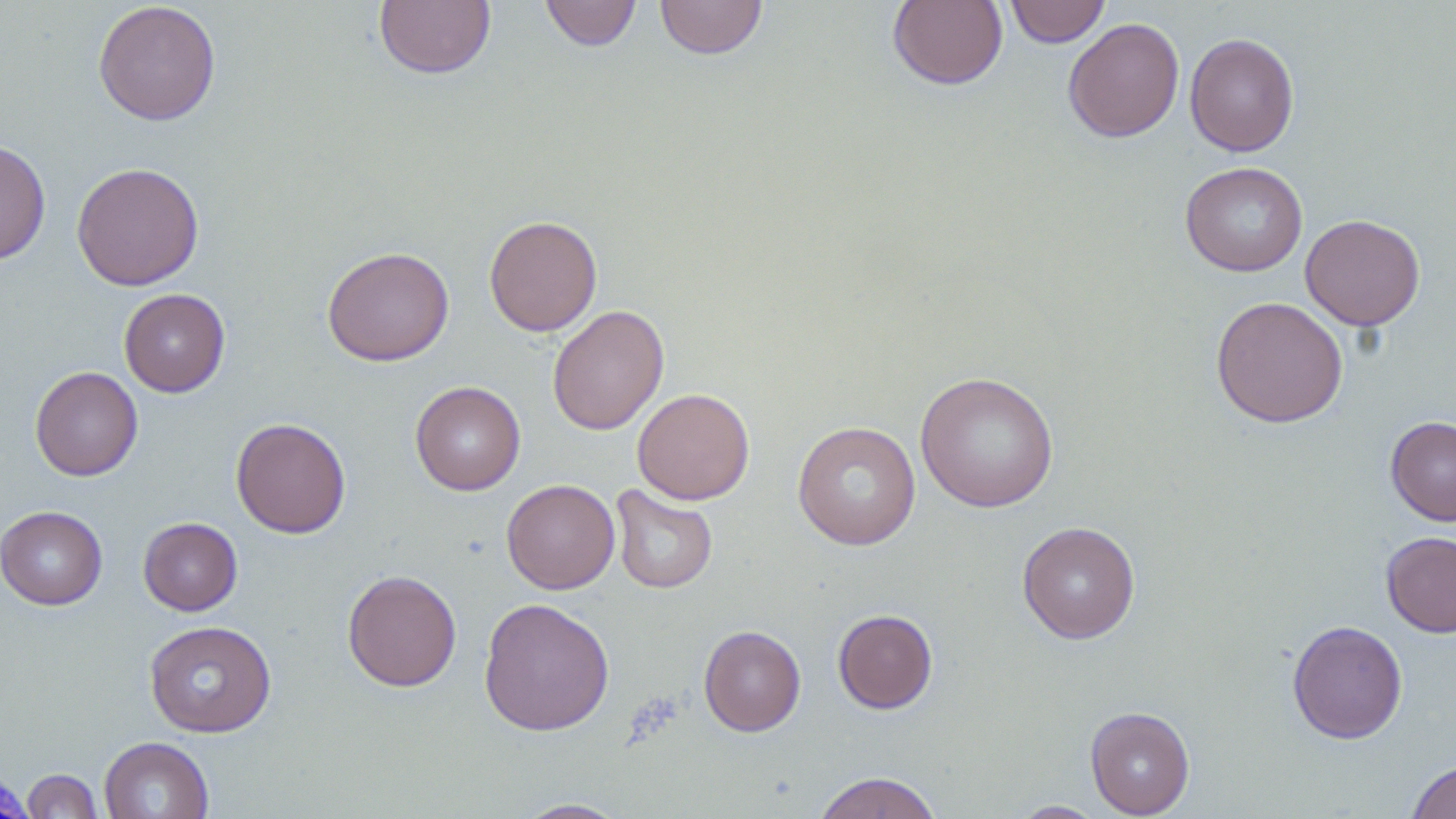

Approximate bounding boxes as [x1, y1, x2, y2] in pixels. Uninfected red blood cell locations: [374, 0, 496, 80], [539, 0, 642, 52], [654, 0, 769, 59], [888, 0, 1008, 90], [1004, 0, 1110, 47], [93, 1, 221, 126], [1063, 18, 1185, 143], [1185, 31, 1299, 157], [0, 139, 51, 266], [71, 161, 204, 291], [1180, 161, 1308, 277], [1300, 213, 1425, 331], [484, 215, 602, 336], [322, 246, 454, 367], [119, 288, 230, 397], [1210, 295, 1348, 428], [547, 304, 669, 435], [30, 366, 143, 481], [915, 371, 1059, 513], [410, 380, 525, 496], [632, 388, 755, 505], [1386, 415, 1456, 526], [230, 417, 351, 538], [792, 421, 921, 550], [501, 479, 620, 594], [609, 485, 718, 594], [0, 505, 108, 610], [138, 517, 242, 615], [1017, 521, 1140, 644], [1380, 531, 1456, 637], [342, 569, 462, 692], [478, 597, 615, 736], [833, 608, 938, 714], [144, 620, 277, 737], [1287, 620, 1407, 744], [699, 625, 806, 736], [1085, 706, 1195, 818], [99, 736, 214, 819], [1406, 758, 1456, 819], [21, 768, 103, 818], [811, 771, 944, 819], [512, 798, 632, 818], [1009, 801, 1107, 818]. Slide-level diagnosis: negative for blood parasites. Single field of view. Optical microscopy. May-Grünwald-Giemsa stain. Image is 1456×819 pixels. Thin blood film. Captured at 1000x magnification.